Report the malaria status of this cell.
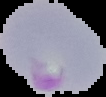
Parasitized.

preparation: thin blood film
image_size: 106×97 pixels
image_type: cell region segmented out of the field of view; surrounding area masked to black